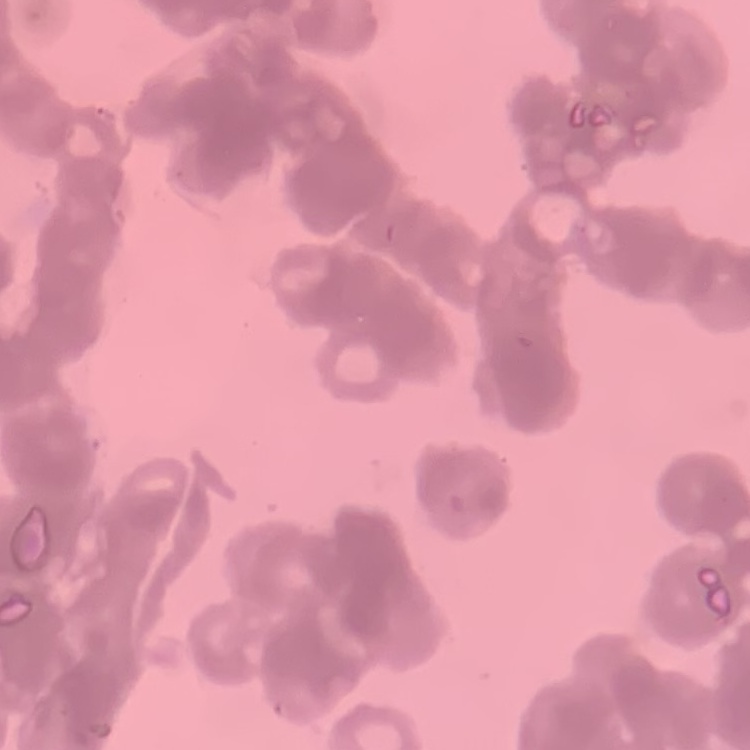

The erythrocytes exhibit rouleaux formation. Thin blood smear. Square crop of a larger photomicrograph. Field's or Giemsa stain.